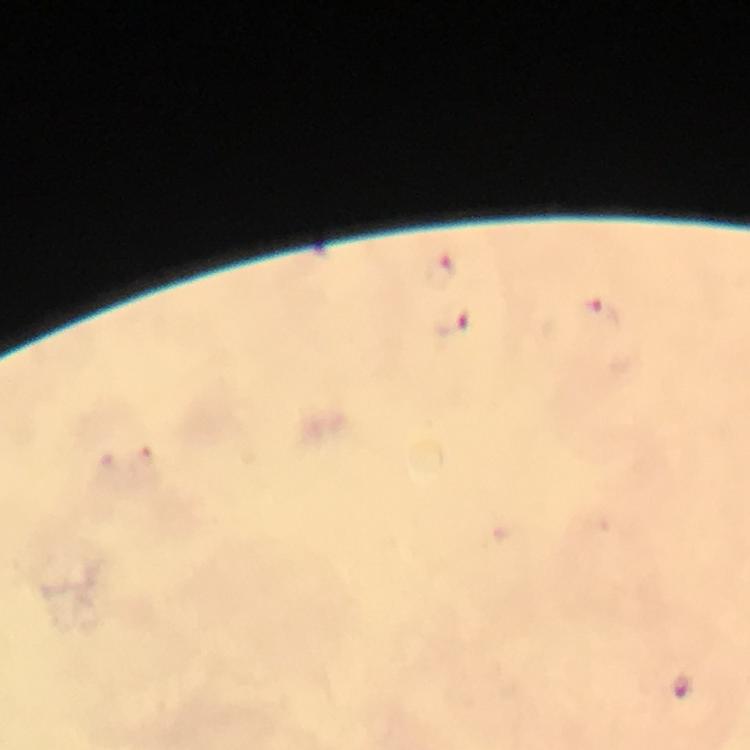

Approximate centers as (x, y) in pixels.
Summary:
  - Plasmodium parasite locations: (442, 271), (602, 320), (452, 322), (679, 685)
  - Image size: 750×750 pixels
  - Immersion oil: used
  - Preparation: thick blood smear
  - Stain: Giemsa
  - Cropped from: one field of view
  - Capture: smartphone photograph through a microscope
  - Magnification: 100x
  - Context: from a malaria diagnostic workup